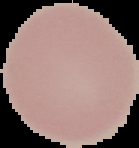
preparation = thin blood film
result = no malaria parasites detected
image size = 139×148 pixels
image type = segmented cell region with the area outside set to black